Classify this cell by malaria status.
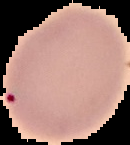
Parasitized.

image type = cell region segmented out of the field of view; surrounding area masked to black
image size = 130×145 pixels
preparation = thin blood smear